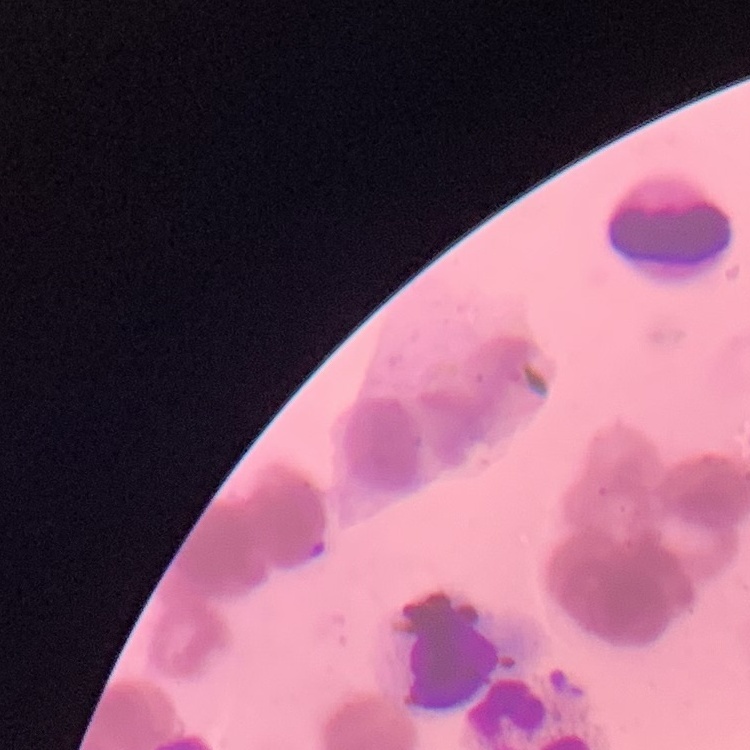

The erythrocytes exhibit rouleaux formation. One tile cut from a larger photomicrograph. Stained with either Field's or Giemsa. Thin blood film.